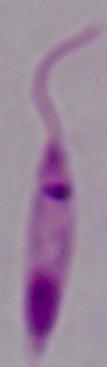
magnification = 1000x
identification = Leishmania
modality = micrograph